Locate every Plasmodium ovale-infected red blood cell.
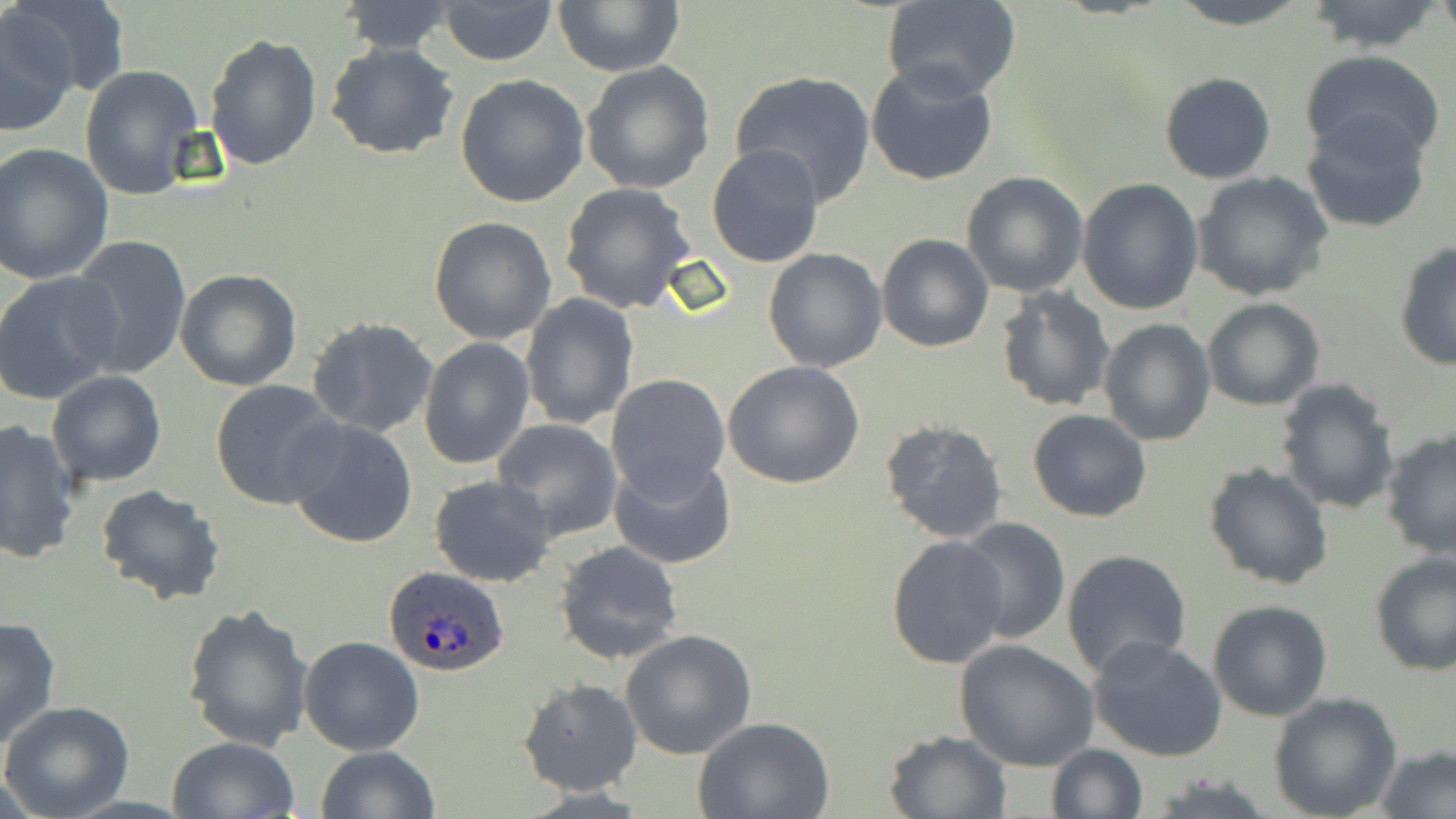

Approximate bounding boxes as [x1, y1, x2, y2] in pixels.
Plasmodium ovale-infected red blood cells: [381, 565, 510, 676].

Uninfected red blood cell locations: [8, 0, 125, 104], [552, 0, 685, 76], [883, 0, 1023, 101], [1162, 0, 1315, 29], [1303, 0, 1443, 53], [436, 1, 557, 66], [338, 2, 461, 54], [1, 9, 80, 133], [204, 34, 324, 174], [325, 42, 459, 161], [1300, 50, 1448, 163], [580, 61, 716, 194], [865, 63, 1000, 187], [80, 65, 203, 199], [729, 69, 877, 205], [1158, 72, 1278, 185], [457, 75, 590, 209], [1301, 112, 1434, 234], [1, 144, 116, 286], [706, 145, 824, 268], [1192, 171, 1333, 301], [961, 172, 1090, 297], [1076, 178, 1204, 316], [559, 182, 697, 316], [429, 216, 557, 345], [876, 233, 993, 353], [68, 236, 192, 377], [1394, 240, 1456, 371], [762, 248, 888, 372], [175, 269, 303, 391], [0, 272, 124, 404], [995, 287, 1116, 414], [518, 293, 638, 431], [1201, 298, 1326, 411], [307, 316, 440, 440], [1098, 319, 1216, 446], [419, 337, 535, 470], [721, 360, 866, 488], [46, 371, 167, 488], [605, 374, 730, 501], [1274, 378, 1401, 519], [210, 380, 344, 510], [1027, 410, 1153, 523], [284, 418, 418, 549], [878, 418, 1010, 543], [493, 419, 623, 541], [0, 421, 80, 564], [1380, 429, 1456, 559], [609, 452, 736, 569], [1202, 462, 1334, 589], [429, 475, 557, 588], [94, 485, 225, 608], [952, 518, 1071, 643], [885, 534, 1010, 671], [554, 540, 687, 667], [1061, 549, 1192, 682], [1369, 553, 1456, 677], [1206, 599, 1333, 722], [180, 602, 314, 751], [0, 615, 61, 751], [620, 630, 757, 760], [1088, 635, 1228, 762], [298, 636, 424, 756], [953, 638, 1101, 772], [518, 679, 643, 798], [1268, 692, 1403, 819], [1, 701, 135, 819], [693, 717, 835, 819], [884, 728, 1013, 819], [167, 737, 300, 819], [1044, 744, 1148, 819], [314, 746, 438, 819], [1377, 747, 1455, 819]. Slide-level diagnosis: Plasmodium ovale. May-Grünwald-Giemsa stain. Optical microscopy. Image is 1456×819 pixels. Captured at 1000x magnification. Thin blood film. Single field of view.